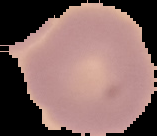
image type = segmented cell region with the area outside set to black
image size = 157×136 pixels
preparation = thin blood film
malaria status = uninfected